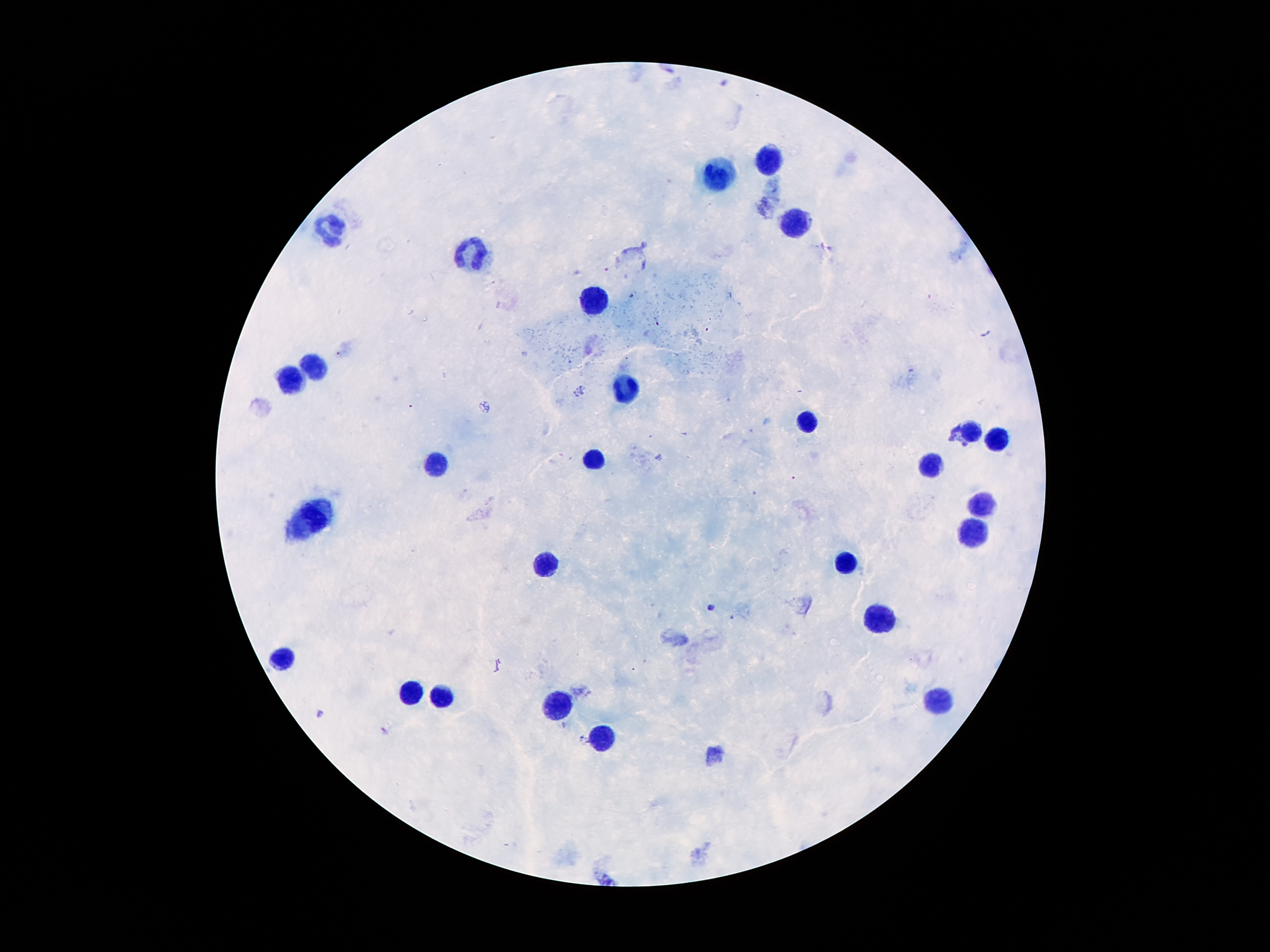
Approximate centers as [x, y] in pixels. Malaria parasite locations: [949, 437], [711, 606], [385, 733]. Leukocyte locations: [771, 156], [716, 176], [796, 222], [334, 230], [470, 257], [596, 302], [311, 367], [292, 381], [626, 390], [808, 423], [972, 430], [997, 440], [596, 455], [430, 465], [932, 469], [981, 503], [309, 520], [976, 536], [546, 565], [842, 566], [884, 616], [281, 656], [412, 689], [441, 700], [556, 700], [939, 700], [603, 734]. Single field of view. Image is 1270×952 pixels. Smartphone photograph taken through the microscope eyepiece. Thick blood film. 100x magnification. Giemsa-stained preparation. Patient malaria status: positive for Plasmodium falciparum.